State which parasite is depicted.
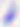

This is Toxoplasma gondii.

modality = photomicrograph
magnification = 400x